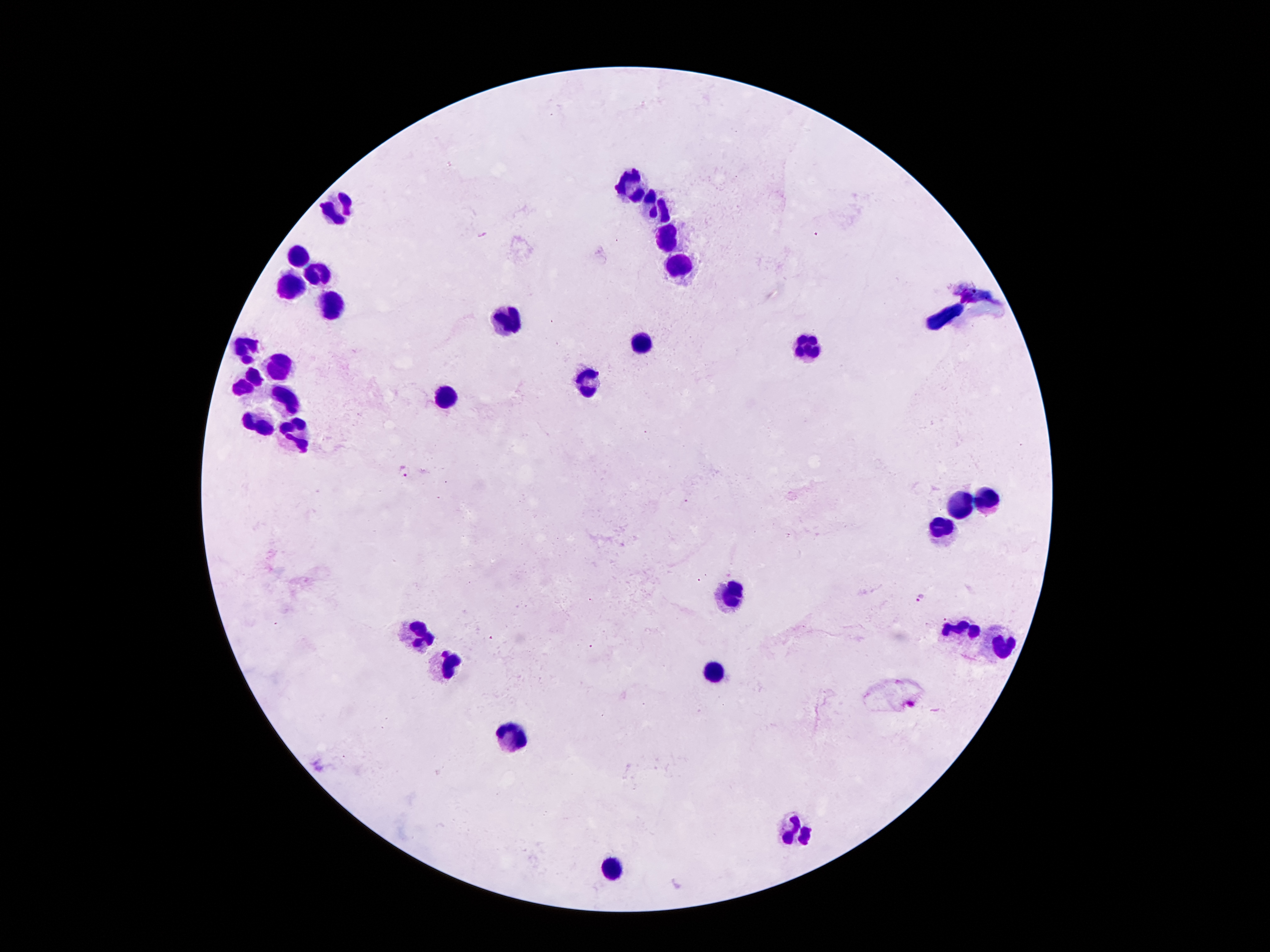 Approximate centers as (x, y) in pixels. Plasmodium parasite locations: (484, 234), (405, 470), (921, 597). Leukocyte locations: (634, 186), (658, 210), (333, 212), (667, 234), (300, 252), (682, 265), (322, 276), (291, 285), (985, 299), (335, 305), (508, 318), (945, 318), (640, 340), (811, 349), (247, 351), (280, 367), (587, 373), (247, 382), (446, 393), (287, 404), (256, 422), (296, 438), (987, 499), (963, 504), (941, 530), (735, 597), (959, 630), (415, 634), (1001, 643), (448, 665), (713, 674), (514, 738), (795, 826), (609, 868). Single field of view. Photographed through the microscope eyepiece with a smartphone camera. 100x magnification. Giemsa-stained preparation. Image is 1270×952 pixels. Patient malaria status: positive for Plasmodium falciparum. Thick blood film.